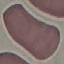

Result: no malaria parasites detected. Thin smear of blood. Giemsa stain. Acquired by smartphone through the microscope eyepiece. Automatically extracted cell patch, resized to 64 × 64 pixels.